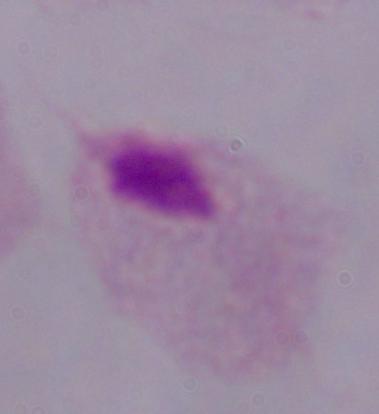
Summary:
  - Identification: trichomonad
  - Modality: micrograph
  - Magnification: 1000x